Describe the morphology of the erythrocytes.
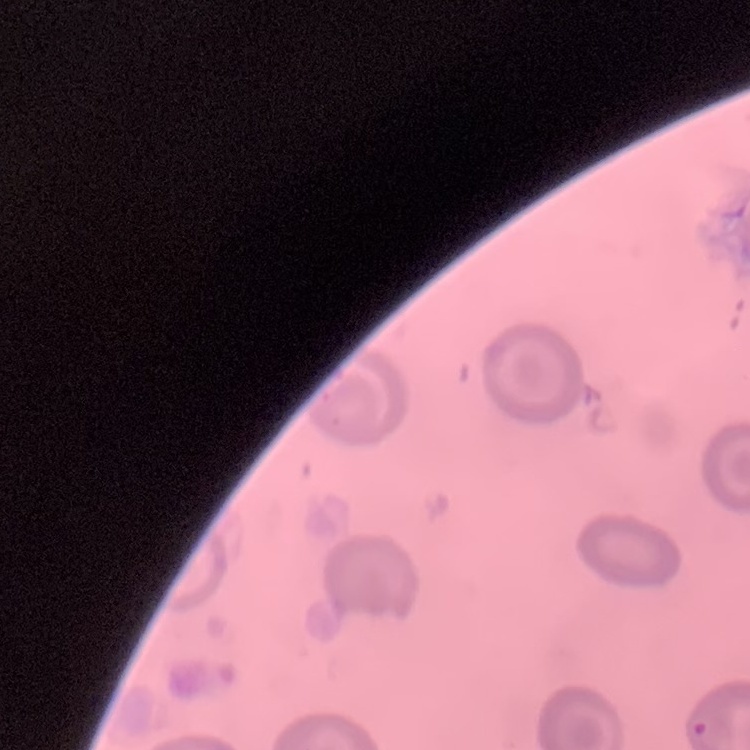
No rouleaux formation.

Square crop of a larger photomicrograph. Field's or Giemsa stain. Thin blood smear.